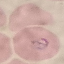

Summary:
  - Malaria status: parasitized
  - Image type: automatically extracted cell patch, resized to 64 × 64 pixels
  - Preparation: thin blood film
  - Capture: smartphone camera at the microscope eyepiece
  - Stain: Giemsa